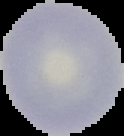
image type = cell region segmented out of the field of view; surrounding area masked to black
result = no malaria parasites detected
preparation = thin blood film
image size = 124×136 pixels